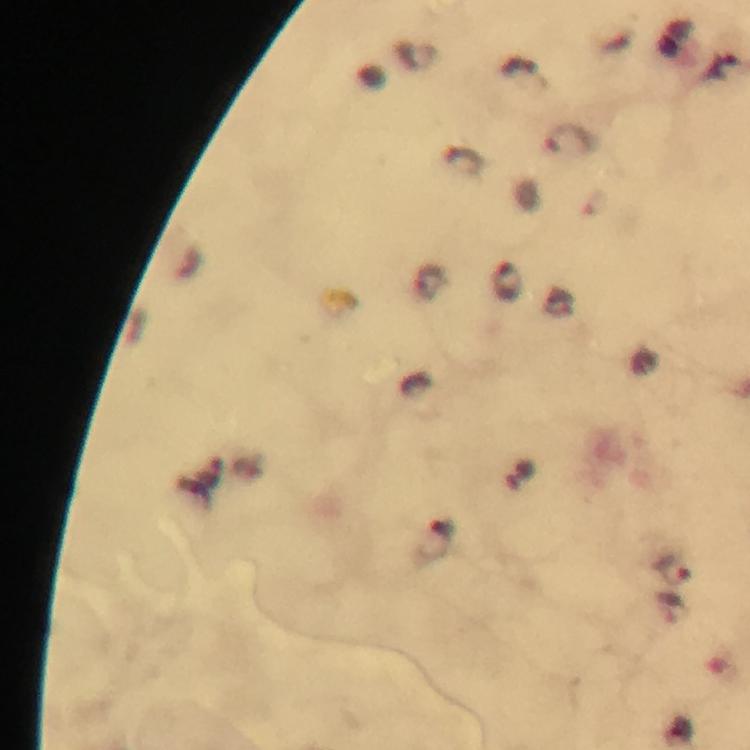
magnification = 100x
preparation = thick smear
capture = smartphone photograph through a microscope
immersion oil = applied
Plasmodium parasite locations = approximate centers as (x, y) in pixels: (572, 140), (677, 571)
cropped from = one field of view
stain = Giemsa
image size = 750×750 pixels
context = from a diagnostic examination for malaria